Comment on the morphology of the erythrocytes.
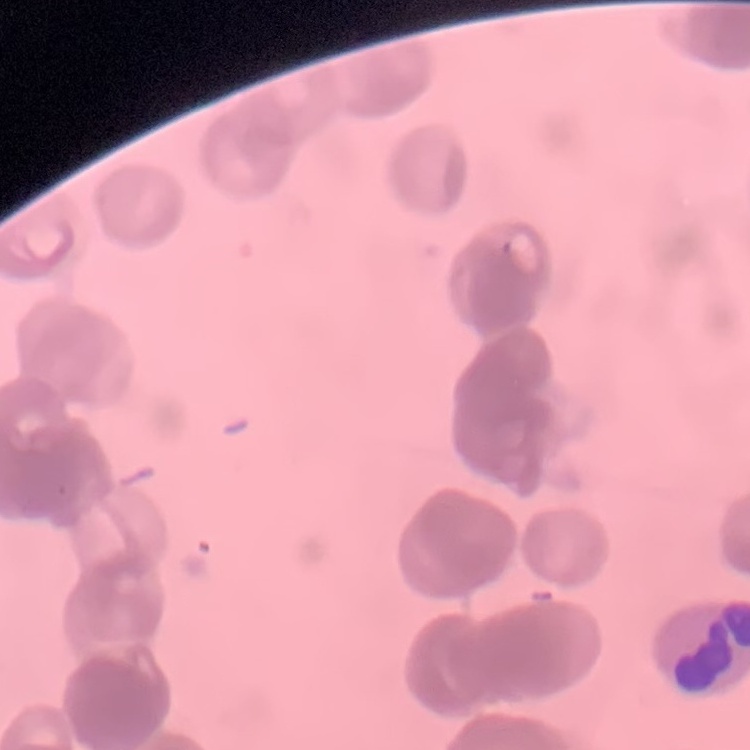
Rouleaux formation.

Thin peripheral smear. Square crop of a larger photomicrograph. Stained with either Field's or Giemsa.